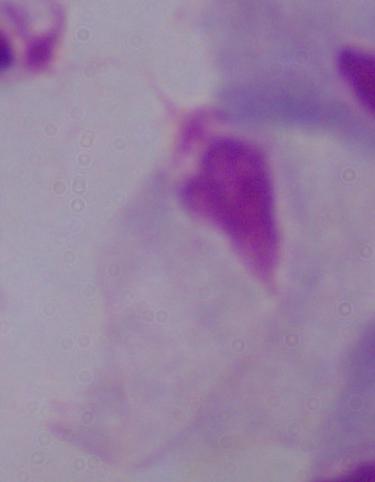
1000x magnification. Photomicrograph. A trichomonad is seen.